Report the malaria status of this cell.
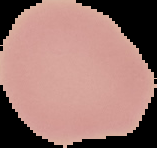

It is uninfected.

preparation = thin blood film
image size = 157×148 pixels
image type = segmented cell region with the area outside set to black